Classify this cell by malaria status.
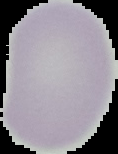

It is uninfected.

{
  "preparation": "thin blood film",
  "image_type": "segmented cell region on a black background",
  "image_size": "118×154 pixels"
}